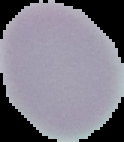
{
  "result": "no malaria parasites seen",
  "image_size": "124×142 pixels",
  "image_type": "cell region segmented out of the field of view; surrounding area masked to black",
  "preparation": "thin blood film"
}